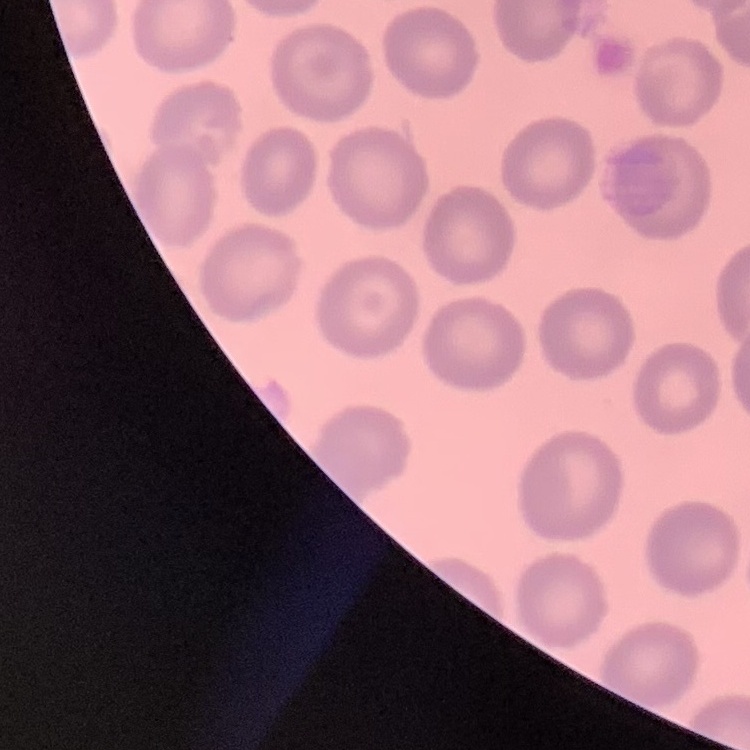

red blood cell morphology = no rouleaux formation
image type = one tile cut from a larger photomicrograph
stain = Field's or Giemsa
preparation = thin blood smear